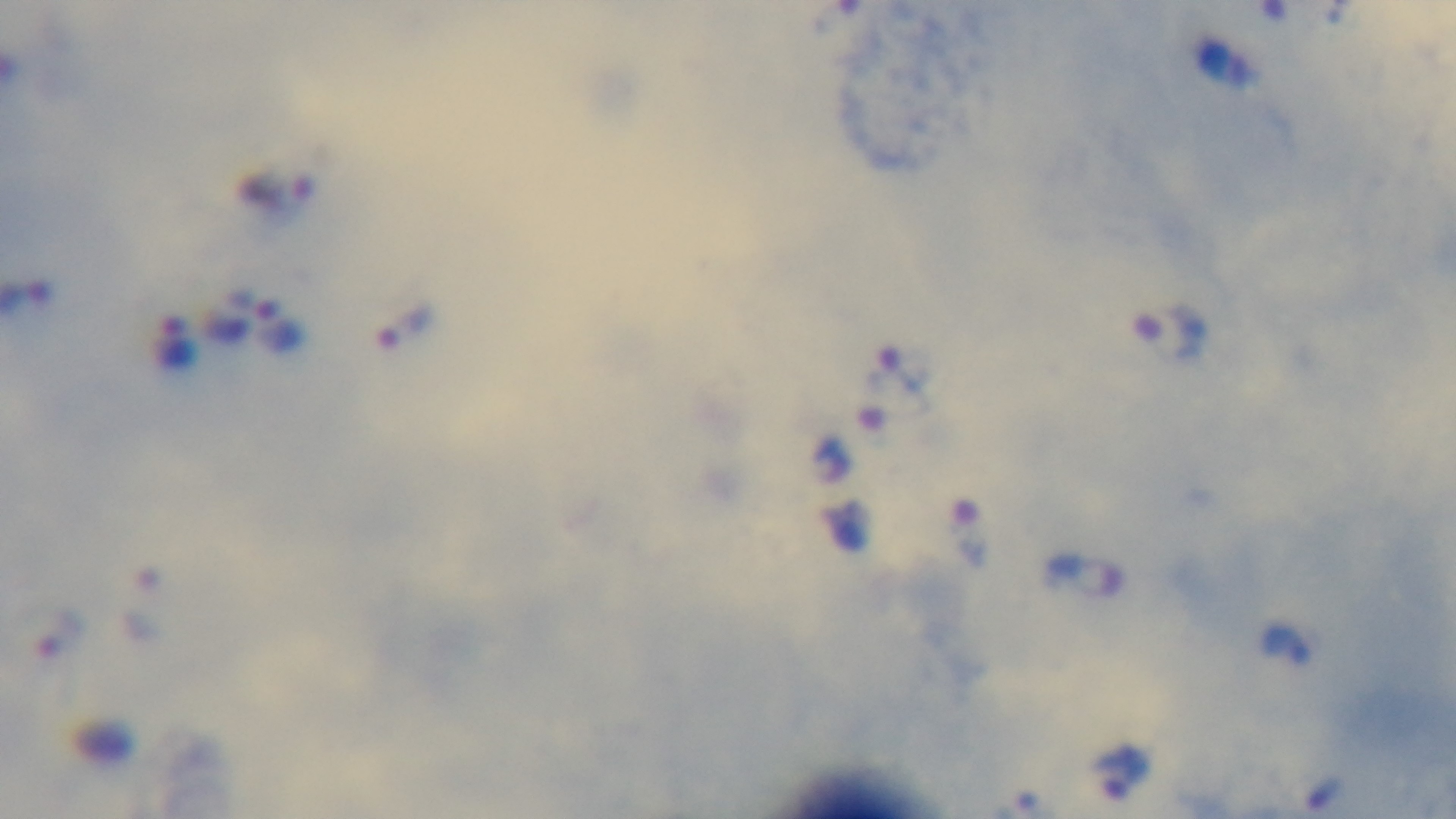
stain = Giemsa
modality = light microscopy
malaria status = positive
preparation = thick blood film
objective = 100x oil immersion
capture = mounted 4K digital camera
field of view = one from the slide